Classify this cell by malaria status.
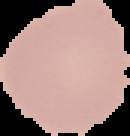
Uninfected.

{
  "preparation": "thin blood film",
  "image_type": "segmented cell region on a black background",
  "image_size": "130×136 pixels"
}